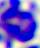
magnification = 400x
modality = photomicrograph
identification = leukocyte